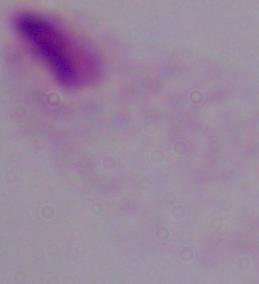
Summary:
  - Modality: micrograph
  - Magnification: 1000x
  - Identification: trichomonad